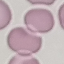

Summary:
  - Result: negative for malaria parasites
  - Capture: smartphone camera at the microscope eyepiece
  - Image type: cell patch, automatically extracted from a larger field of view and resized to 64 × 64 pixels
  - Preparation: thin blood film
  - Stain: Giemsa